Identify the parasite.
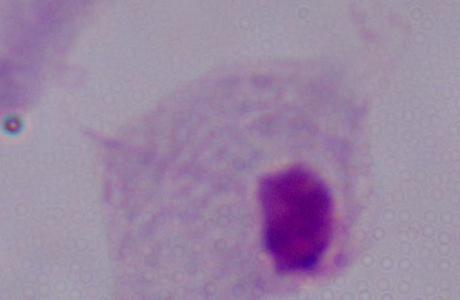
This is a trichomonad.

Micrograph. 1000x magnification.